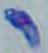
Summary:
  - Magnification: 1000x
  - Identification: Toxoplasma gondii
  - Modality: micrograph